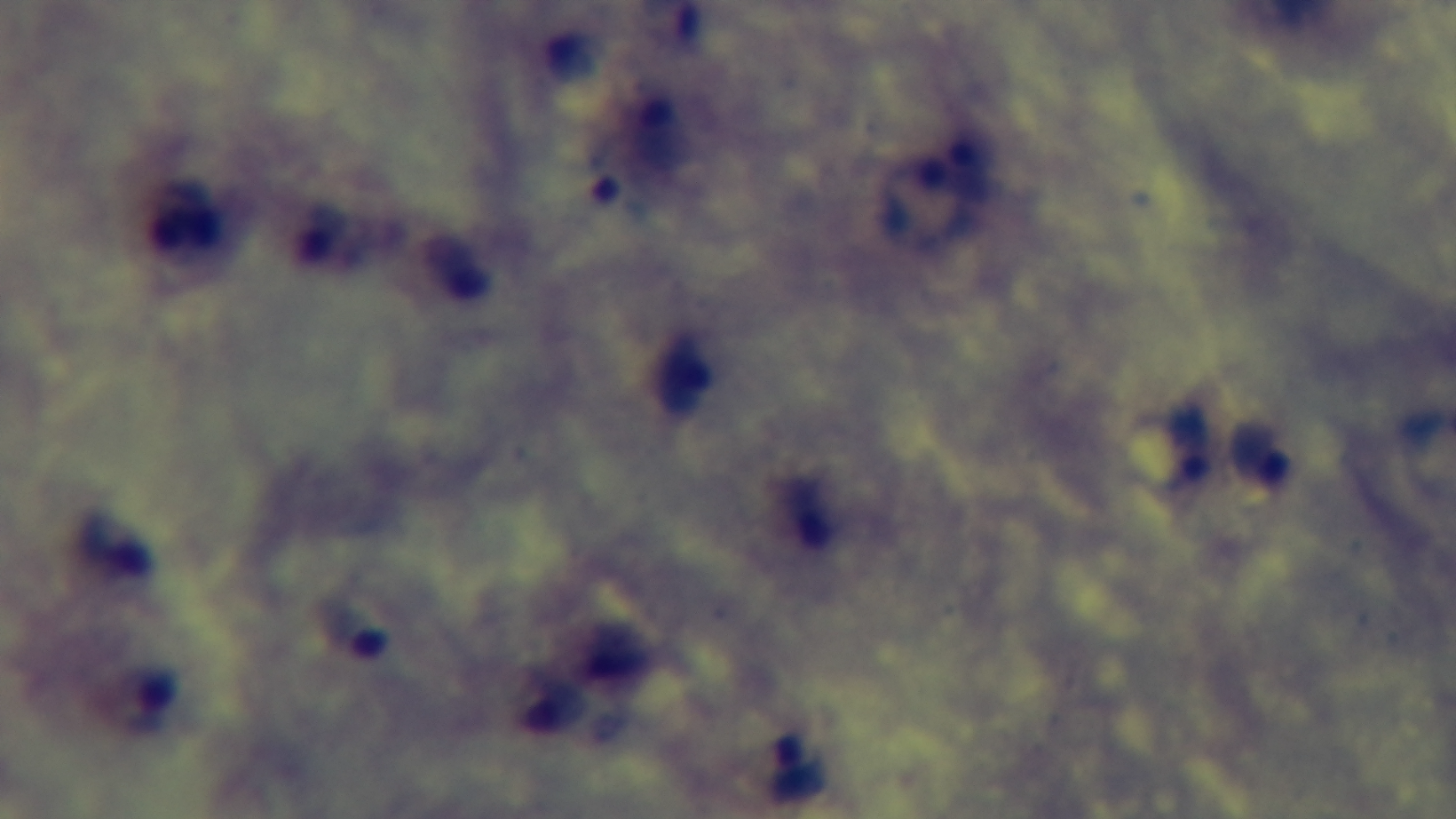

Single field of view. Malaria status: positive. Preparation: thick smear. Giemsa-stained. Light microscopy. Mounted 4K digital camera. 100x oil-immersion objective.